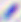

Micrograph. Toxoplasma gondii is seen. 400x magnification.